Locate every blood parasite and identify its species.
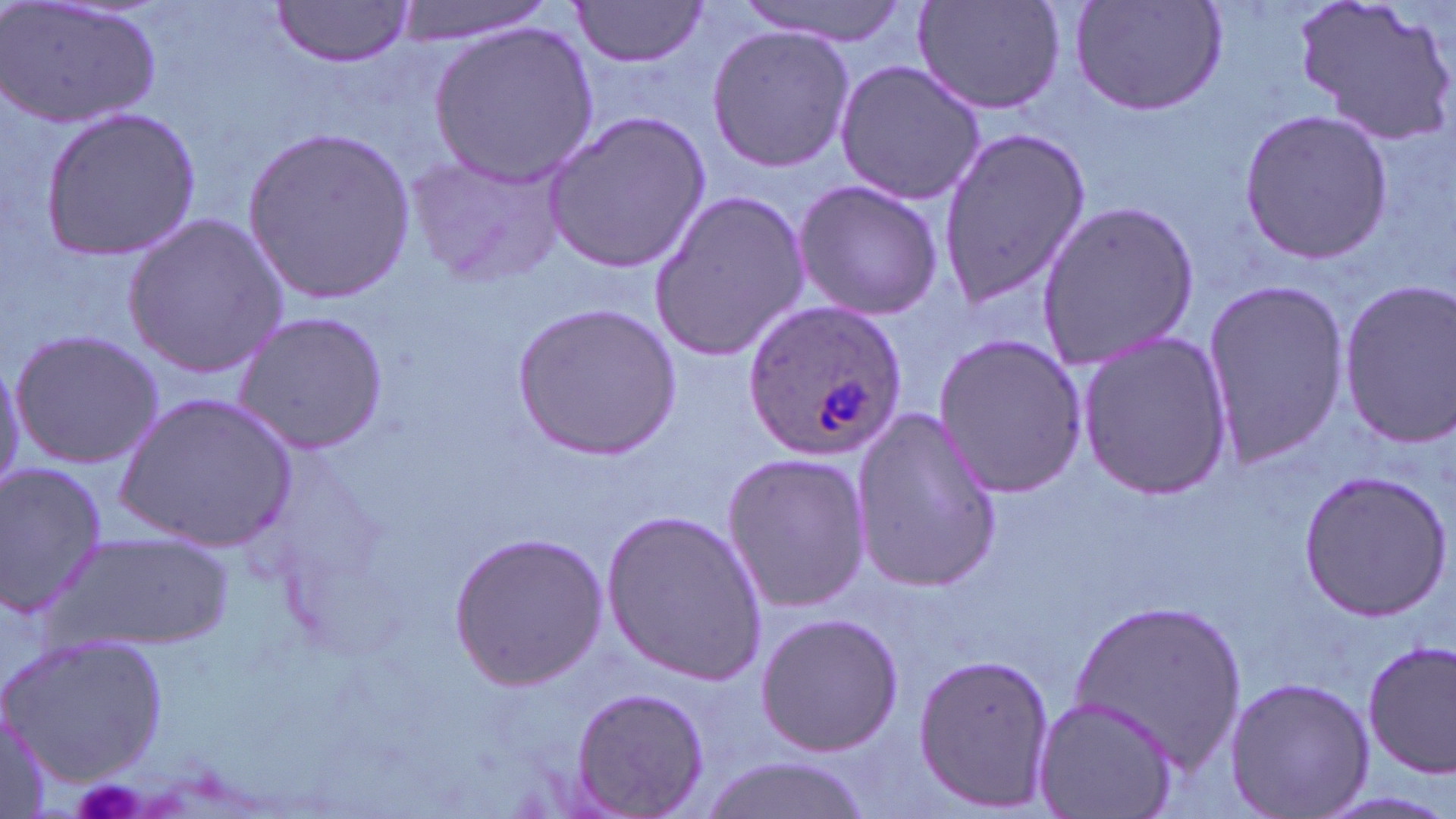

Approximate bounding boxes as named x1/y1/x2/y2 corners in pixels.
Plasmodium ovale-infected red blood cells: (x1=741, y1=301, x2=911, y2=459).
No Plasmodium falciparum, Plasmodium malariae, Plasmodium vivax, Babesia divergens, or Trypanosoma brucei observed.

slide_level_diagnosis: Plasmodium ovale
stain: May-Grünwald-Giemsa
field_of_view: single
uninfected_red_blood_cell_locations: 'approximate bounding boxes as named x1/y1/x2/y2 corners in pixels: (x1=3, y1=0, x2=160, y2=130), (x1=387, y1=0, x2=553, y2=44), (x1=733, y1=0, x2=915, y2=44), (x1=911, y1=0, x2=1069, y2=117), (x1=1067, y1=0, x2=1231, y2=118), (x1=1295, y1=0, x2=1455, y2=148), (x1=269, y1=1, x2=416, y2=66), (x1=570, y1=1, x2=709, y2=72), (x1=428, y1=21, x2=599, y2=186), (x1=704, y1=23, x2=853, y2=173), (x1=833, y1=57, x2=988, y2=207), (x1=39, y1=107, x2=202, y2=260), (x1=542, y1=108, x2=711, y2=274), (x1=1239, y1=109, x2=1394, y2=262), (x1=243, y1=123, x2=414, y2=303), (x1=937, y1=126, x2=1093, y2=309), (x1=402, y1=146, x2=567, y2=288), (x1=791, y1=179, x2=944, y2=322), (x1=649, y1=186, x2=810, y2=363), (x1=1037, y1=199, x2=1203, y2=375), (x1=122, y1=211, x2=288, y2=379), (x1=1200, y1=272, x2=1355, y2=476), (x1=1335, y1=278, x2=1456, y2=449), (x1=513, y1=302, x2=680, y2=457), (x1=232, y1=312, x2=387, y2=454), (x1=1074, y1=329, x2=1232, y2=501), (x1=8, y1=330, x2=162, y2=468), (x1=932, y1=332, x2=1088, y2=500), (x1=0, y1=351, x2=24, y2=493), (x1=115, y1=393, x2=298, y2=552), (x1=850, y1=407, x2=1001, y2=591), (x1=720, y1=450, x2=874, y2=613), (x1=0, y1=462, x2=110, y2=623), (x1=1298, y1=468, x2=1450, y2=622), (x1=601, y1=509, x2=768, y2=684), (x1=52, y1=528, x2=238, y2=651), (x1=449, y1=531, x2=607, y2=689), (x1=1069, y1=595, x2=1245, y2=771), (x1=753, y1=611, x2=906, y2=759), (x1=3, y1=633, x2=169, y2=784), (x1=1361, y1=640, x2=1456, y2=777), (x1=911, y1=652, x2=1058, y2=812), (x1=1226, y1=675, x2=1373, y2=816), (x1=570, y1=686, x2=710, y2=816), (x1=1035, y1=695, x2=1177, y2=819), (x1=0, y1=696, x2=58, y2=819), (x1=695, y1=755, x2=878, y2=819)'
modality: light microscopy
magnification: 1000x
preparation: thin blood smear
image_size: 1456×819 pixels